Classify this cell by malaria status.
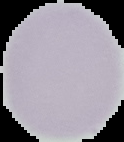

Uninfected.

Image is 124×142 pixels. The area outside the segmented cell region is set to black. From a thin blood smear.